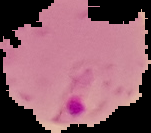

Image is 151×133 pixels. From a thin blood smear. Segmented cell region on a black background. Result: Plasmodium parasites detected.